Outline each blood parasite and name the species.
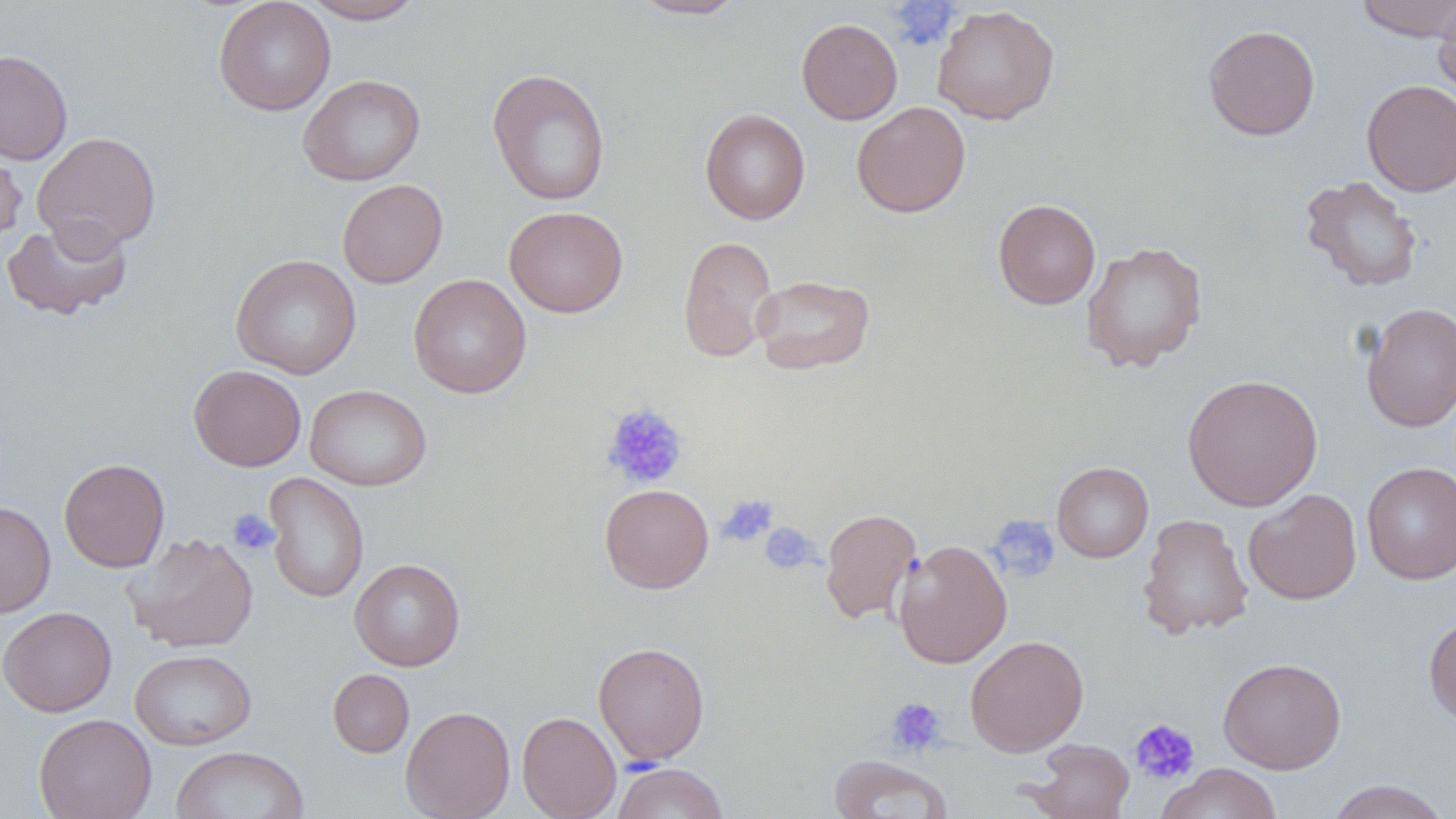

No blood parasites seen.

Summary:
  - Coordinate format: approximate bounding boxes as [x1, y1, x2, y2] in pixels
  - Uninfected red blood cell locations: [213, 0, 336, 116], [300, 0, 425, 24], [628, 0, 748, 20], [1353, 0, 1456, 42], [1433, 0, 1456, 102], [931, 5, 1060, 125], [796, 18, 902, 124], [1203, 24, 1321, 140], [0, 49, 73, 165], [487, 68, 611, 206], [298, 74, 425, 186], [1361, 80, 1456, 197], [851, 101, 970, 217], [700, 108, 811, 224], [32, 132, 161, 253], [0, 141, 27, 247], [1300, 175, 1423, 292], [337, 179, 448, 288], [993, 199, 1101, 309], [504, 205, 628, 317], [1, 217, 133, 322], [678, 235, 779, 362], [1081, 241, 1207, 372], [231, 254, 361, 379], [408, 274, 531, 398], [750, 274, 875, 375], [1361, 302, 1456, 432], [189, 364, 306, 471], [1182, 373, 1323, 511], [305, 384, 432, 491], [58, 458, 169, 572], [1052, 461, 1154, 562], [1362, 461, 1456, 585], [263, 472, 369, 604], [599, 483, 714, 593], [1243, 488, 1362, 605], [0, 501, 56, 618], [820, 507, 922, 624], [1137, 513, 1253, 639], [124, 532, 259, 653], [893, 538, 1012, 669], [350, 558, 465, 671], [0, 606, 117, 717], [1423, 614, 1456, 727], [965, 635, 1089, 756], [593, 642, 710, 765], [130, 648, 257, 750], [1218, 657, 1347, 774], [328, 669, 414, 758], [400, 706, 515, 819], [517, 711, 621, 819], [34, 713, 157, 819], [1025, 738, 1135, 818], [171, 746, 309, 819], [829, 754, 954, 818], [612, 762, 728, 819], [1156, 763, 1283, 819], [1325, 780, 1453, 819]
  - Platelet locations: [887, 2, 960, 51], [602, 404, 689, 490], [719, 494, 778, 547], [227, 509, 280, 556], [988, 515, 1061, 583], [760, 522, 820, 575], [886, 697, 947, 756], [1129, 718, 1200, 785]
  - Slide-level diagnosis: no evidence of blood parasites
  - Field of view: one of a larger specimen
  - Image size: 1456×819 pixels
  - Preparation: thin blood smear
  - Stain: May-Grünwald-Giemsa
  - Modality: light microscopy
  - Magnification: 1000x